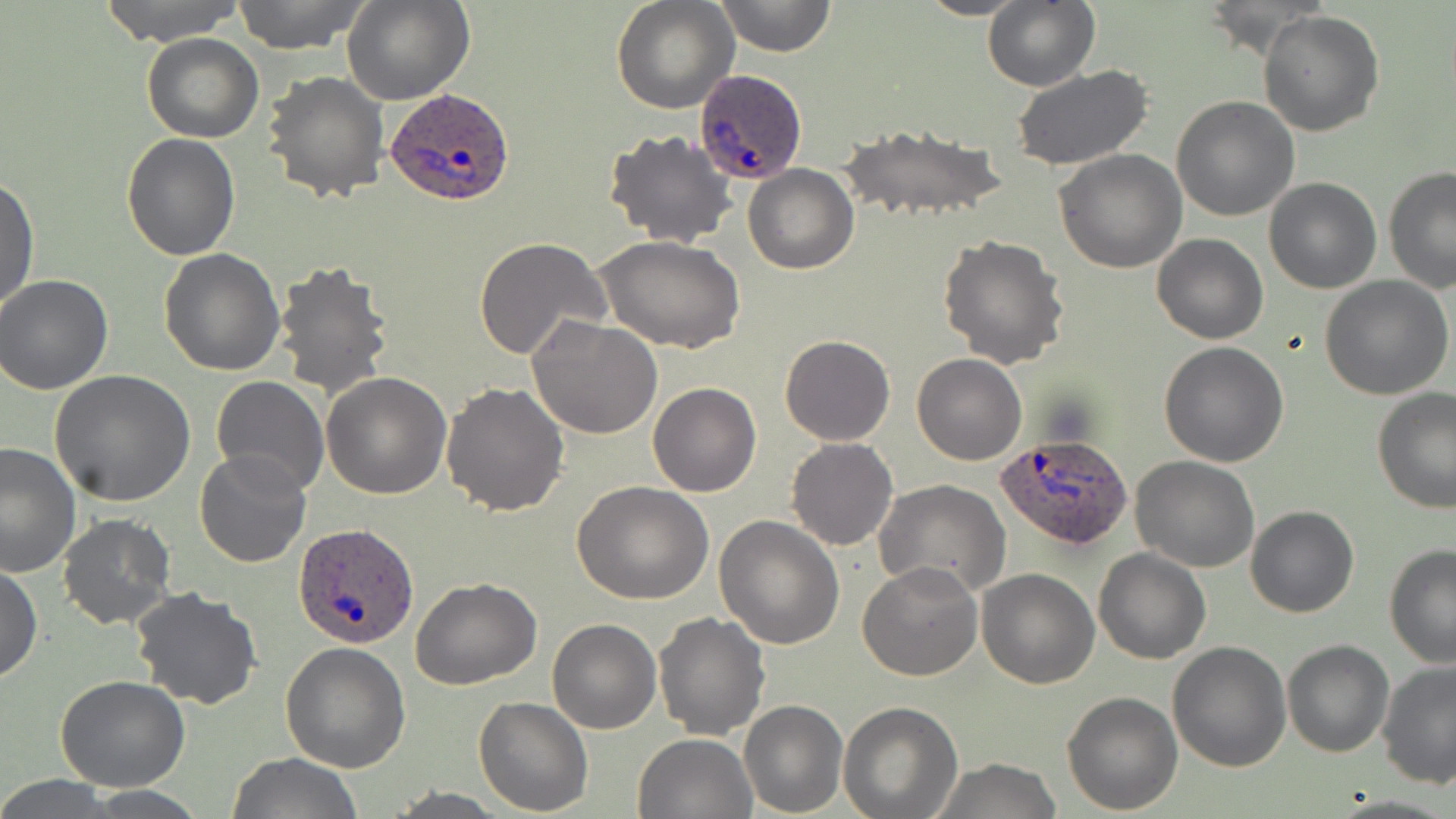 Approximate bounding boxes as (x1, y1, x2, y2) in pixels. Uninfected red blood cell locations: (95, 0, 248, 46), (231, 0, 371, 53), (344, 0, 474, 105), (612, 0, 738, 113), (713, 0, 837, 57), (914, 0, 1031, 20), (983, 2, 1099, 90), (1259, 11, 1384, 137), (142, 32, 265, 143), (1010, 65, 1153, 168), (264, 71, 389, 203), (1171, 96, 1300, 222), (839, 122, 1006, 225), (604, 130, 738, 248), (121, 132, 240, 259), (1054, 150, 1187, 274), (742, 165, 859, 274), (1383, 166, 1456, 294), (1, 174, 38, 313), (1264, 176, 1381, 293), (1153, 234, 1268, 343), (939, 236, 1070, 369), (475, 237, 611, 360), (599, 237, 744, 354), (158, 248, 286, 375), (273, 260, 396, 400), (1321, 274, 1453, 399), (0, 275, 112, 394), (528, 315, 663, 440), (780, 334, 895, 446), (1158, 341, 1290, 466), (912, 353, 1027, 465), (51, 370, 194, 506), (322, 370, 452, 498), (210, 376, 328, 496), (441, 382, 569, 518), (648, 382, 761, 497), (1373, 390, 1456, 514), (786, 438, 897, 551), (0, 441, 81, 579), (193, 449, 311, 569), (1130, 455, 1259, 572), (874, 480, 1011, 599), (573, 481, 713, 604), (1246, 505, 1360, 618), (56, 512, 178, 630), (713, 515, 844, 648), (1384, 543, 1456, 668), (1093, 548, 1211, 664), (858, 561, 982, 681), (0, 564, 43, 681), (976, 568, 1098, 688), (411, 575, 542, 689), (129, 586, 263, 711), (652, 611, 771, 739), (547, 619, 662, 734), (1281, 639, 1395, 757), (281, 641, 412, 773), (1168, 642, 1293, 772), (1375, 662, 1456, 789), (55, 676, 189, 792), (1062, 689, 1183, 812), (474, 696, 594, 816), (739, 700, 849, 817), (839, 702, 964, 818), (632, 731, 757, 819), (225, 752, 364, 819), (928, 758, 1064, 818), (0, 775, 121, 818), (79, 787, 210, 817). Plasmodium ovale-infected red blood cell locations: (695, 70, 808, 185), (385, 87, 515, 207), (997, 433, 1133, 550), (294, 521, 418, 647). Slide-level diagnosis: Plasmodium ovale. 1000x magnification. Image is 1456×819 pixels. Thin blood smear. May-Grünwald-Giemsa stain. Optical microscopy. Single field of view.